Locate every blood parasite and identify its species.
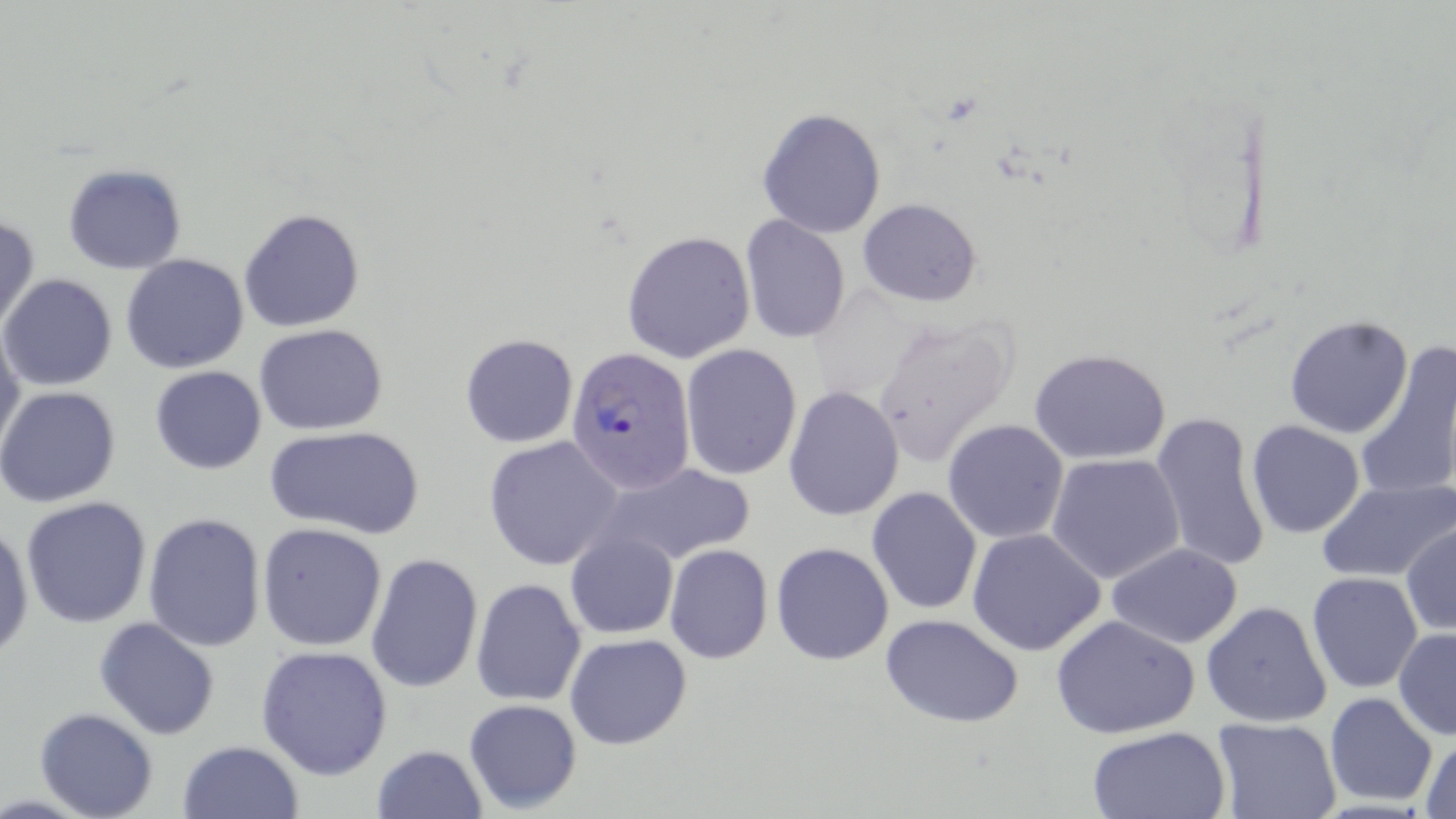
Approximate bounding boxes as (x1,y1)-(x2,y2) corner pairs in pixels.
Plasmodium falciparum-infected red blood cells: (566,347)-(697,494).
No Plasmodium ovale, Plasmodium malariae, Plasmodium vivax, Babesia divergens, or Trypanosoma brucei observed.

Uninfected red blood cell locations: (757,107)-(886,238), (63,164)-(186,274), (857,198)-(983,306), (239,208)-(365,332), (1,214)-(40,334), (740,216)-(851,343), (621,229)-(755,363), (121,254)-(249,374), (1,274)-(117,391), (869,311)-(1022,470), (1284,314)-(1414,439), (0,323)-(25,460), (254,323)-(389,435), (459,334)-(579,448), (1355,340)-(1456,501), (679,343)-(803,481), (1029,348)-(1174,462), (150,365)-(267,474), (0,385)-(121,508), (783,386)-(904,521), (1151,412)-(1272,574), (942,417)-(1069,544), (1246,419)-(1365,538), (263,425)-(425,539), (483,437)-(624,572), (1046,452)-(1186,584), (591,463)-(758,568), (1316,478)-(1456,582), (866,488)-(982,615), (20,495)-(153,629), (144,513)-(267,653), (0,522)-(34,664), (257,522)-(388,651), (1401,522)-(1455,636), (966,527)-(1104,655), (567,532)-(679,639), (770,542)-(894,666), (1105,543)-(1245,650), (664,544)-(773,664), (365,553)-(483,693), (1306,571)-(1424,693), (470,578)-(587,708), (1200,600)-(1332,728), (880,613)-(1026,728), (1052,614)-(1202,740), (94,618)-(221,739), (1392,629)-(1456,741), (564,632)-(693,750), (256,645)-(393,779), (1323,693)-(1438,808), (463,699)-(583,813), (34,708)-(158,819), (1210,716)-(1343,819), (1085,725)-(1230,817), (1418,732)-(1456,819), (177,740)-(305,819), (370,743)-(487,818). Slide-level diagnosis: Plasmodium falciparum. Single field of view. May-Grünwald-Giemsa stain. Image is 1456×819 pixels. Thin blood smear. Captured at 1000x magnification. Optical microscopy.